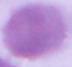

magnification: 1000x
modality: micrograph
identification: erythrocyte